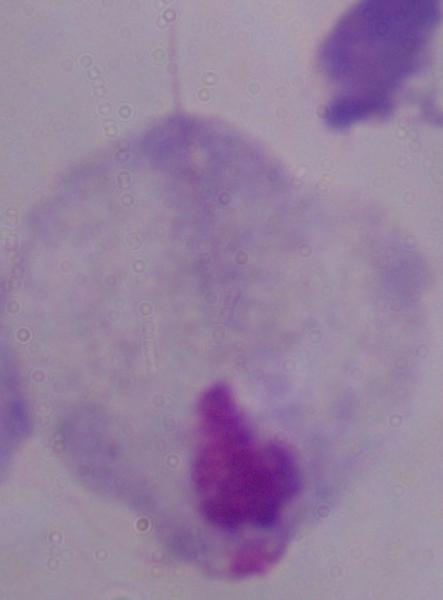

modality = micrograph
identification = trichomonad
magnification = 1000x